Assess this cell for malaria.
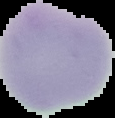
Uninfected.

image_size: 115×118 pixels
preparation: thin blood smear
image_type: segmented cell region on a black background